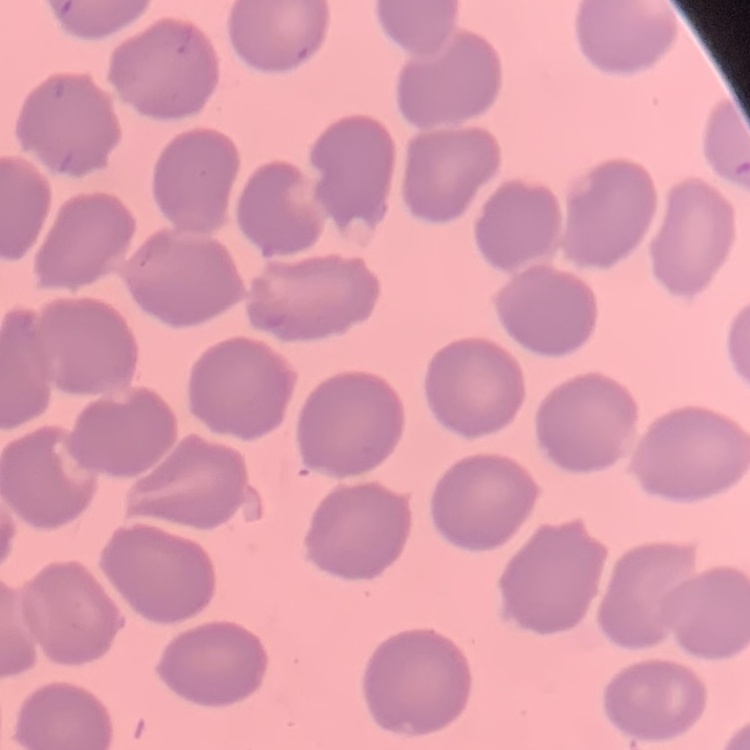
erythrocyte morphology = no rouleaux formation
preparation = thin peripheral smear
stain = Field's or Giemsa
image type = square crop of a larger photomicrograph